Report the malaria status.
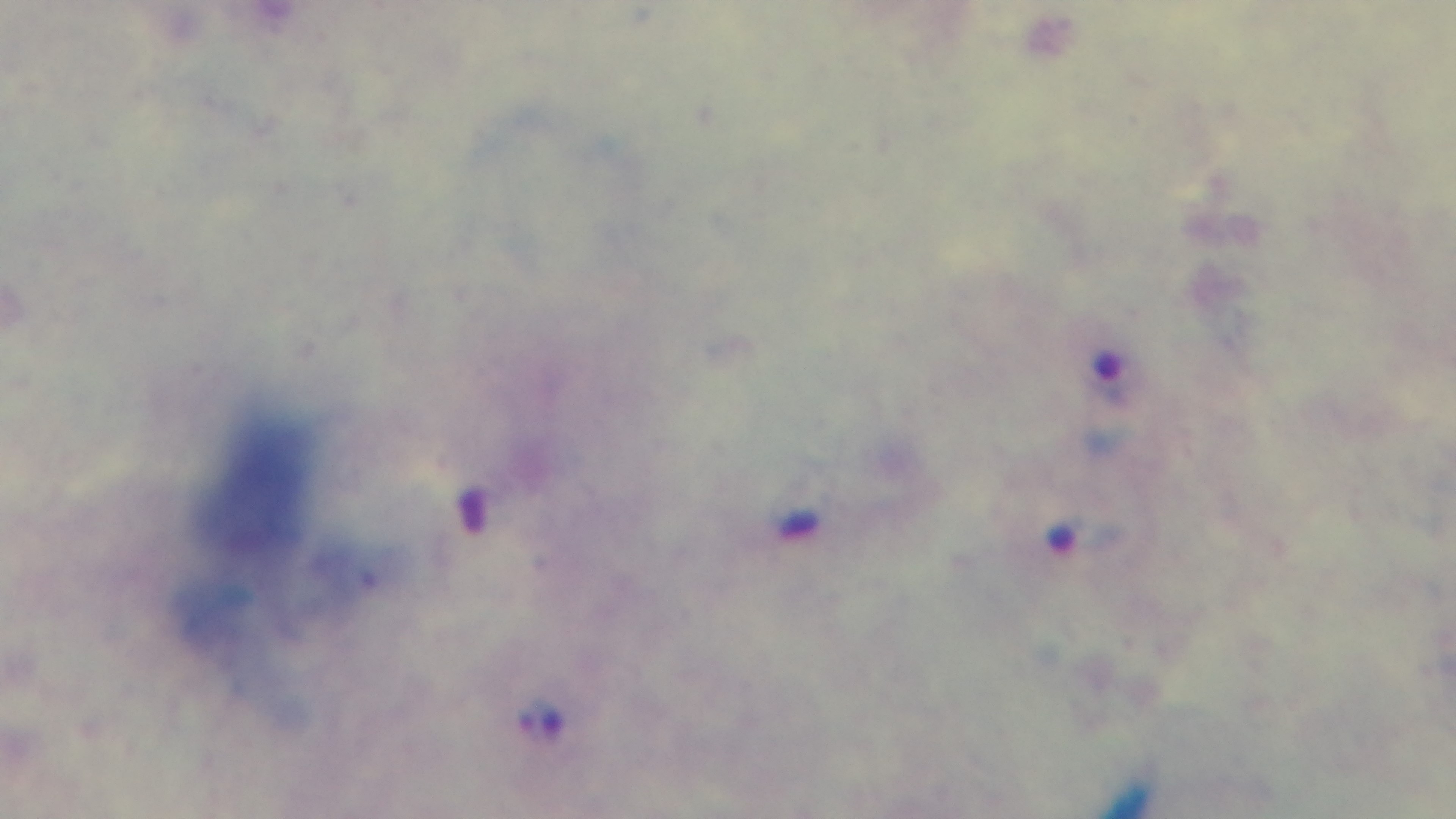

Positive.

stain: Giemsa
capture: mounted 4K digital camera
preparation: thick
field_of_view: single
objective: 100x oil immersion
modality: light microscopy